Classify this cell by malaria status.
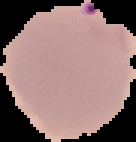

Parasitized.

image type = segmented cell region with the area outside set to black
image size = 136×142 pixels
preparation = thin blood film